Give the position of every leukocyte visible.
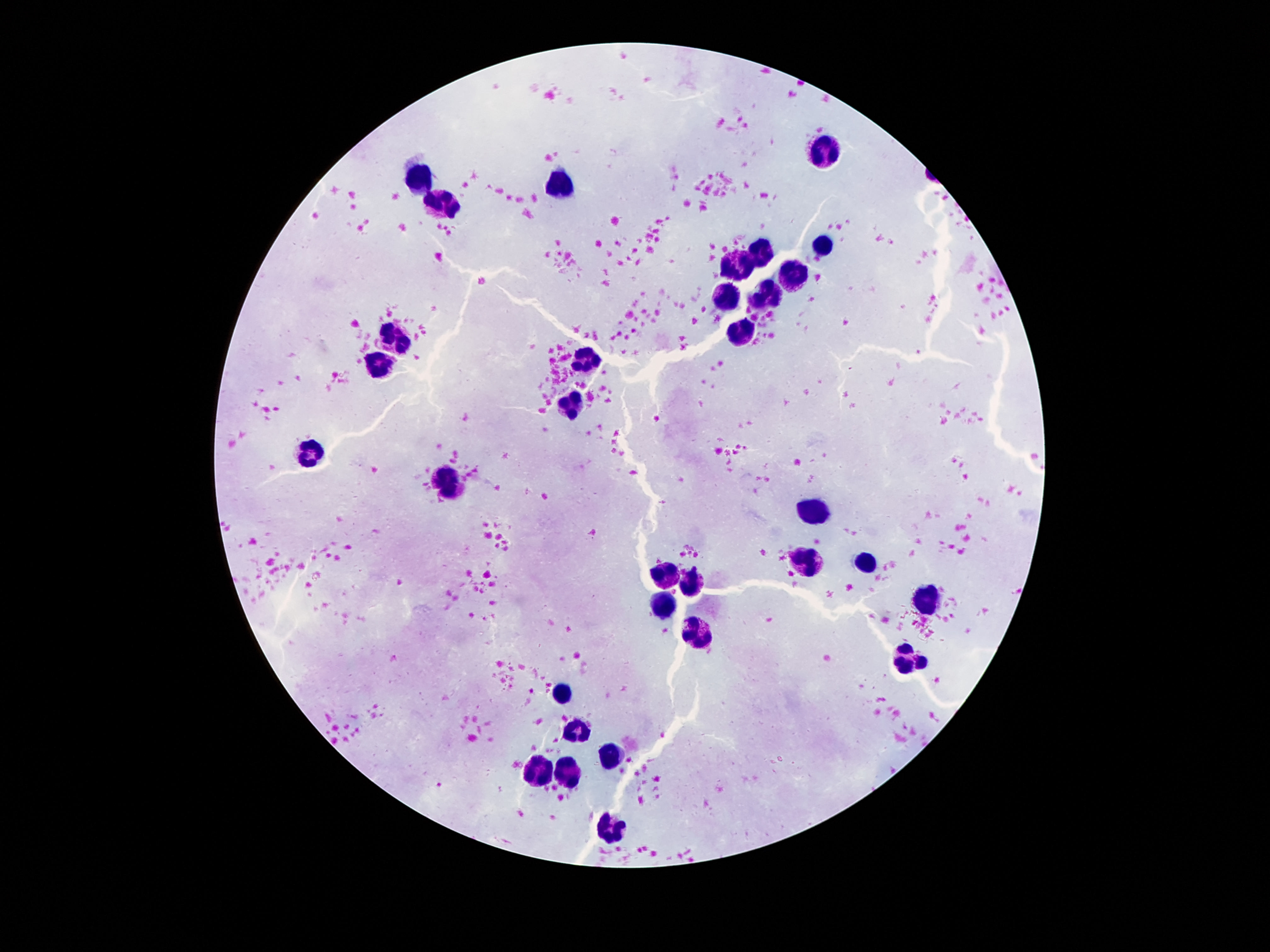

Approximate centers as {x, y} in pixels.
Leukocytes: {827, 153}, {420, 172}, {560, 185}, {440, 203}, {822, 246}, {761, 257}, {741, 266}, {799, 273}, {732, 294}, {773, 294}, {745, 333}, {397, 336}, {587, 356}, {381, 363}, {573, 402}, {311, 453}, {447, 479}, {819, 509}, {807, 560}, {868, 560}, {662, 572}, {687, 582}, {926, 599}, {664, 603}, {699, 631}, {906, 661}, {562, 691}, {580, 728}, {608, 758}, {535, 771}, {570, 773}, {610, 827}.

patient malaria status = negative
stain = Giemsa
field of view = one from this slide
capture = smartphone camera through the microscope eyepiece
magnification = 100x
preparation = thick blood film
image size = 1270×952 pixels